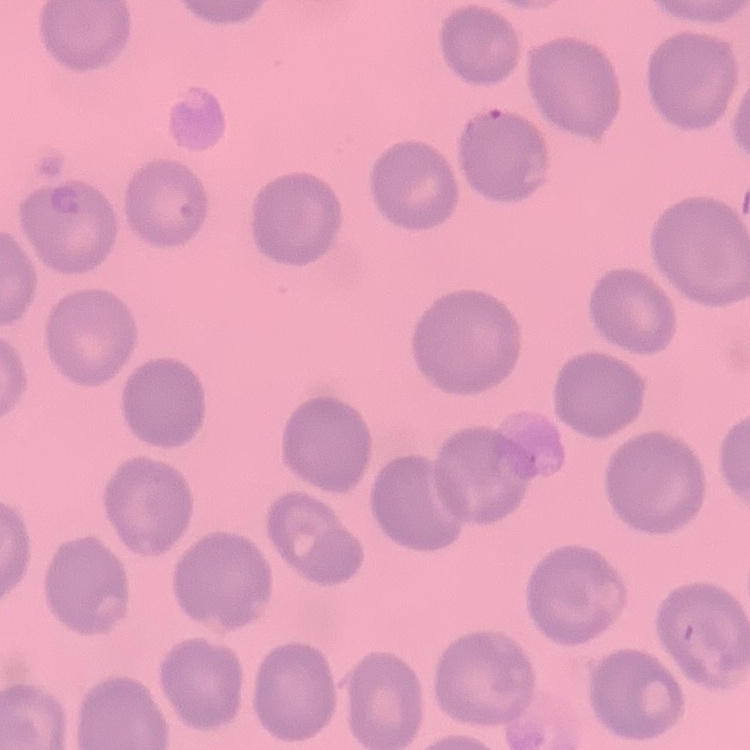
{
  "erythrocyte_morphology": "no rouleaux formation",
  "preparation": "thin blood film",
  "stain": "Field's or Giemsa",
  "image_type": "square crop of a larger photomicrograph"
}